Comment on the morphology of the red blood cells.
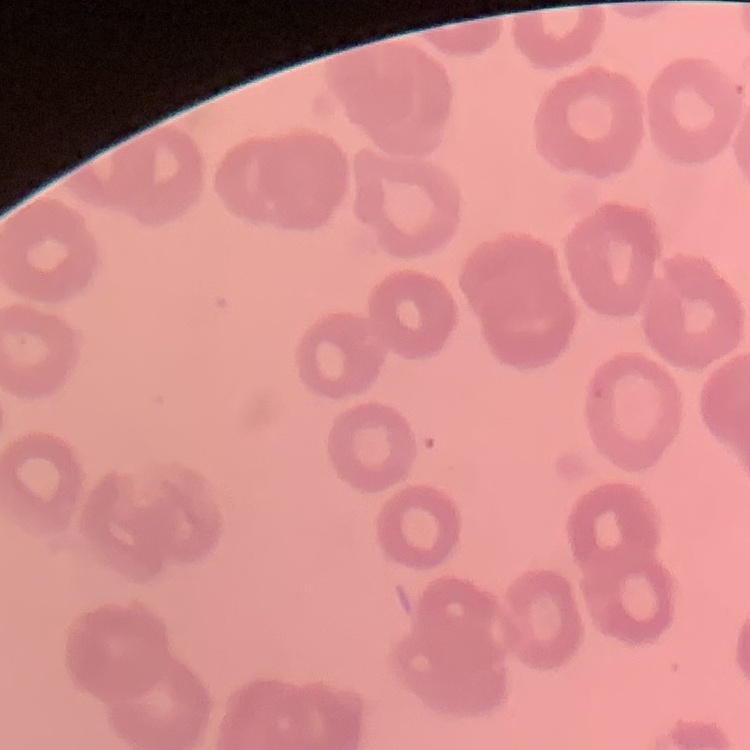

No rouleaux formation.

Summary:
  - Image type: one tile cut from a larger photomicrograph
  - Stain: Field's or Giemsa
  - Preparation: thin peripheral smear